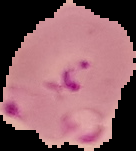
The area outside the segmented cell region is set to black. Image is 136×151 pixels. From a thin blood smear. Result: Plasmodium parasites detected.